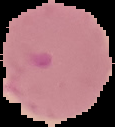

Segmented cell region on a black background. Image is 115×127 pixels. From a thin blood film. Malaria status: parasitized.